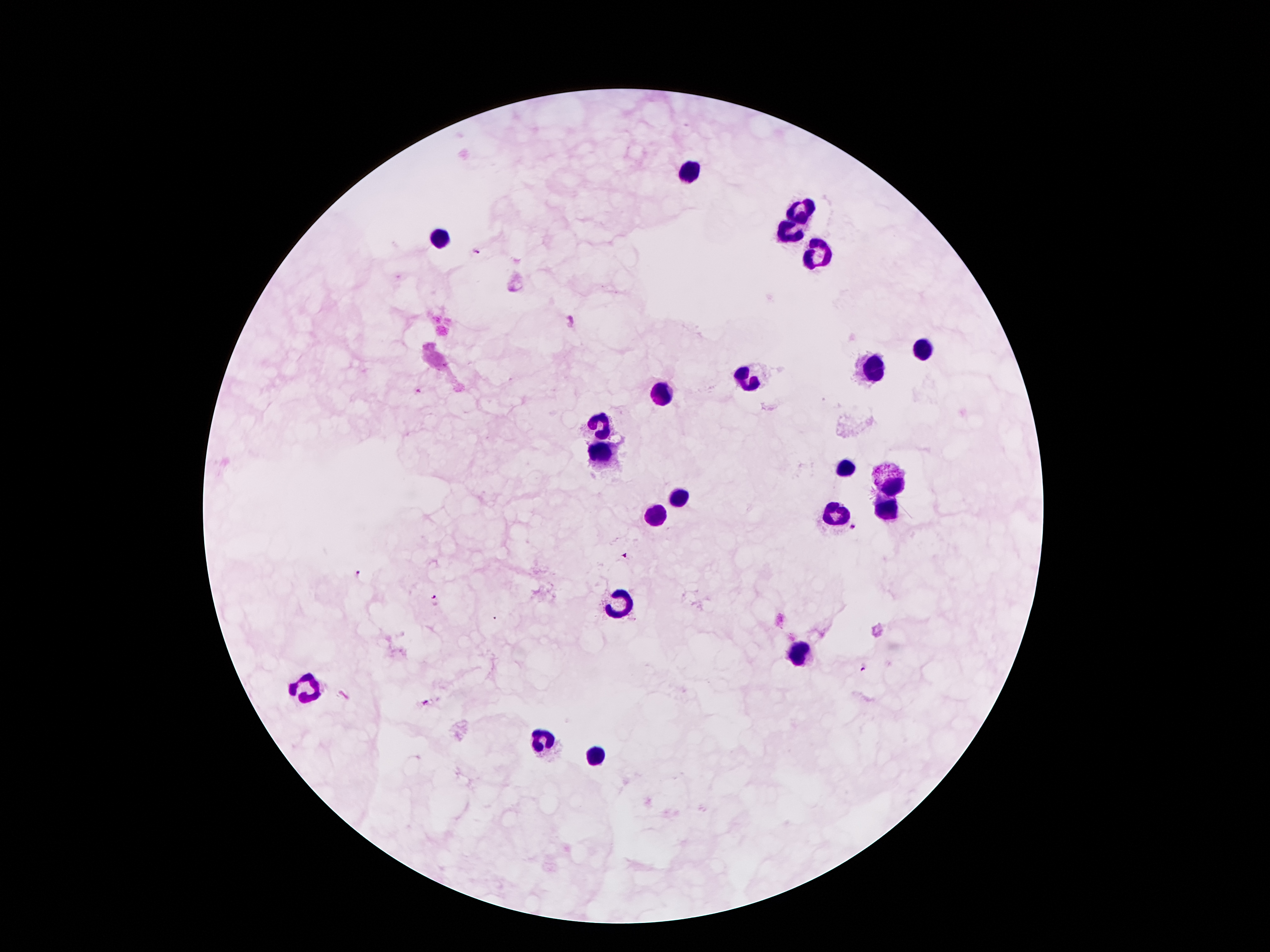
Approximate centers as {x, y} in pixels. Leukocyte locations: {690, 170}, {799, 214}, {785, 228}, {441, 239}, {814, 250}, {923, 348}, {875, 370}, {748, 380}, {661, 392}, {601, 422}, {599, 454}, {846, 468}, {893, 480}, {679, 497}, {886, 509}, {836, 513}, {654, 514}, {620, 598}, {800, 652}, {307, 684}, {544, 742}, {595, 754}. Plasmodium parasite locations: {476, 251}, {418, 391}, {854, 526}, {625, 555}, {357, 572}, {433, 599}, {863, 666}, {426, 703}. Photographed through the microscope eyepiece with a smartphone camera. Giemsa stain. Patient malaria status: infected with Plasmodium falciparum. Thick peripheral-blood smear. One field from this slide. Image is 1270×952 pixels. 100x magnification.